Point out each leukocyte.
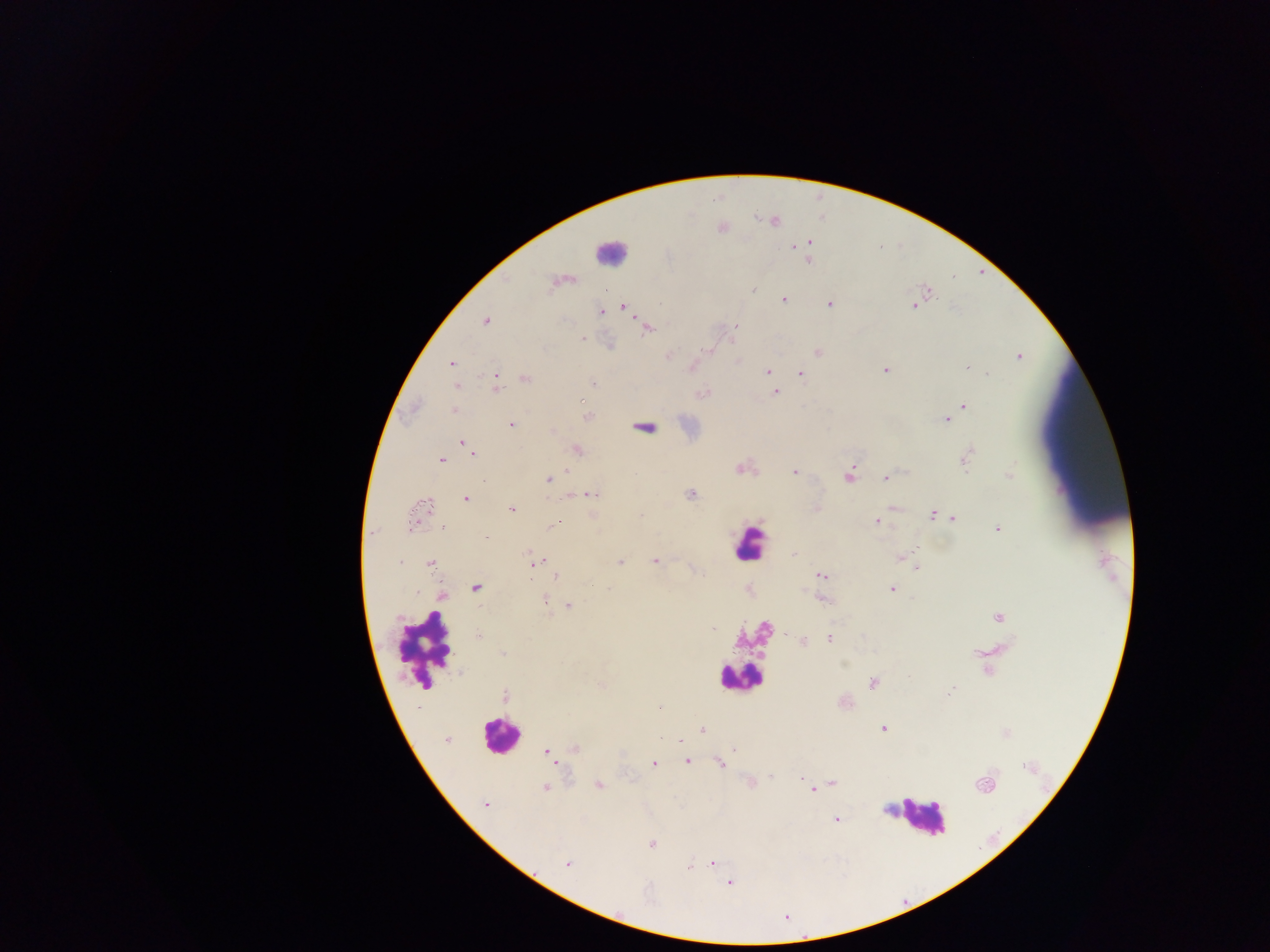
Approximate centers as {x, y} in pixels.
Leukocytes: {610, 251}, {748, 543}, {426, 648}, {740, 678}, {500, 735}, {920, 816}.

malaria_parasite_locations: 'approximate centers as {x, y} in pixels: {774, 221}, {810, 243}, {794, 247}, {808, 260}, {556, 282}, {752, 290}, {929, 292}, {784, 300}, {829, 304}, {914, 305}, {623, 307}, {601, 311}, {486, 321}, {736, 325}, {647, 329}, {581, 338}, {703, 350}, {818, 351}, {667, 356}, {1018, 356}, {451, 364}, {967, 368}, {885, 370}, {767, 372}, {800, 373}, {987, 373}, {525, 379}, {592, 383}, {496, 385}, {457, 387}, {775, 392}, {703, 393}, {583, 400}, {964, 406}, {455, 411}, {588, 417}, {946, 420}, {512, 424}, {461, 442}, {468, 448}, {577, 449}, {473, 452}, {966, 457}, {442, 460}, {740, 468}, {567, 470}, {795, 472}, {1009, 475}, {849, 477}, {885, 478}, {549, 480}, {482, 481}, {592, 495}, {690, 495}, {466, 498}, {425, 505}, {893, 507}, {816, 508}, {511, 509}, {641, 514}, {932, 514}, {953, 518}, {877, 522}, {411, 524}, {552, 526}, {443, 529}, {998, 529}, {794, 555}, {901, 556}, {655, 561}, {539, 562}, {400, 563}, {620, 563}, {430, 564}, {917, 568}, {556, 576}, {822, 576}, {476, 588}, {608, 588}, {892, 589}, {416, 592}, {443, 595}, {544, 600}, {824, 601}, {568, 606}, {998, 617}, {713, 629}, {786, 633}, {478, 635}, {830, 638}, {803, 641}, {503, 653}, {873, 684}, {602, 686}, {951, 691}, {505, 696}, {660, 706}, {883, 729}, {702, 730}, {446, 739}, {681, 740}, {574, 748}, {734, 749}, {546, 751}, {553, 760}, {687, 762}, {654, 764}, {719, 764}, {801, 778}, {750, 782}, {832, 783}, {599, 785}, {985, 785}, {546, 788}, {813, 790}, {486, 804}, {835, 819}, {652, 843}, {712, 863}, {567, 864}, {690, 866}, {729, 883}'
capture: mobile-phone photograph through a microscope
preparation: thick blood film
field_of_view: single
country: Ghana
image_size: 1270×952 pixels